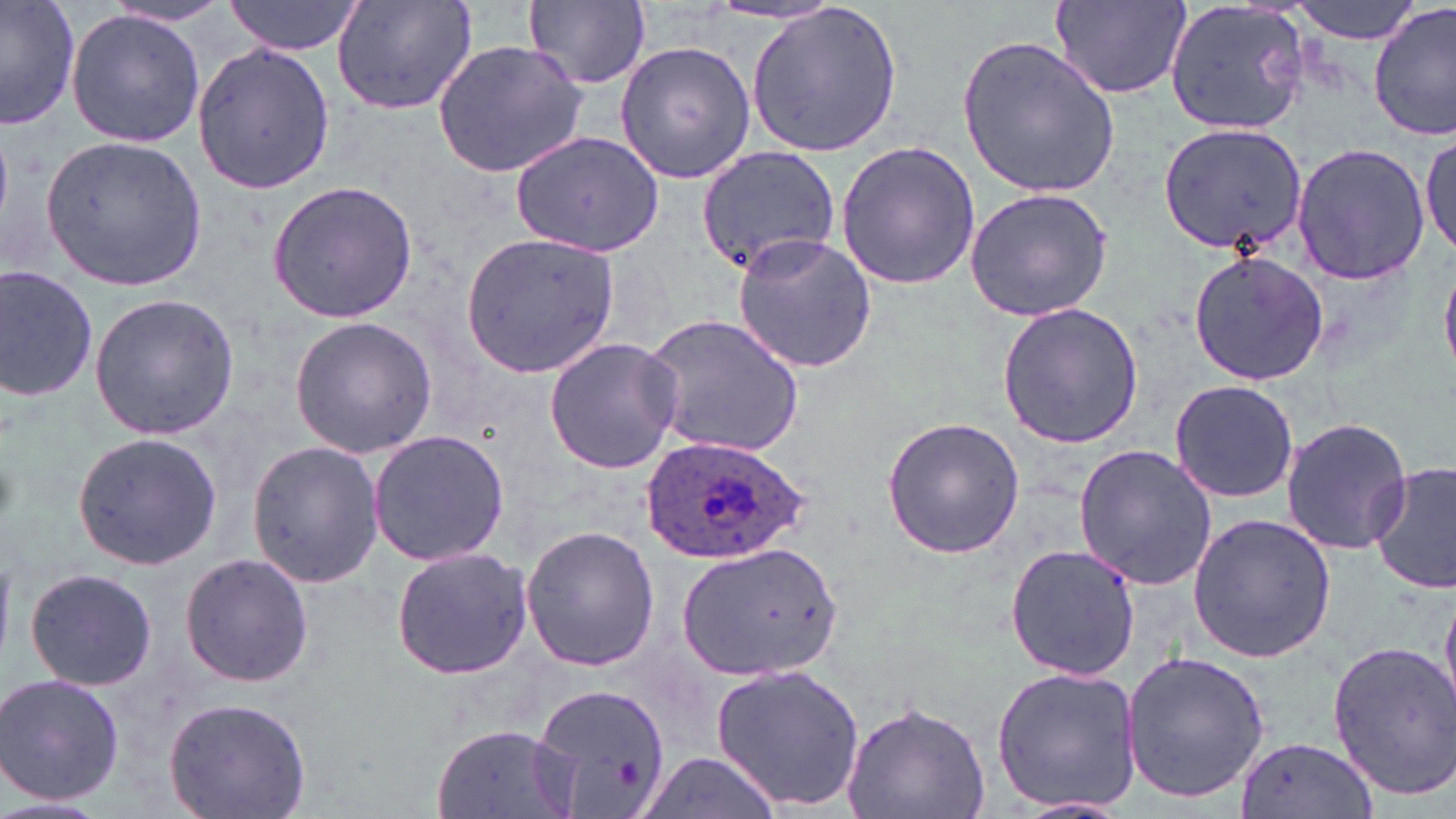
Approximate bounding boxes as [x1, y1, x2, y2] in pixels. Uninfected red blood cell locations: [0, 0, 78, 133], [223, 0, 369, 56], [332, 0, 480, 118], [1288, 0, 1424, 44], [99, 1, 235, 30], [522, 1, 654, 93], [1164, 1, 1313, 137], [1051, 2, 1190, 99], [746, 4, 904, 157], [1371, 4, 1455, 141], [66, 10, 206, 147], [956, 35, 1119, 200], [614, 38, 757, 184], [431, 39, 590, 178], [191, 42, 335, 196], [1157, 121, 1307, 255], [511, 129, 665, 256], [1419, 130, 1454, 261], [38, 132, 209, 292], [834, 140, 982, 291], [1290, 142, 1431, 286], [692, 144, 841, 277], [266, 180, 417, 323], [963, 187, 1115, 323], [460, 231, 621, 377], [732, 234, 879, 373], [1189, 250, 1331, 387], [0, 266, 98, 401], [87, 293, 241, 441], [995, 301, 1143, 449], [644, 313, 807, 457], [289, 315, 438, 459], [543, 336, 682, 474], [1168, 380, 1298, 502], [882, 417, 1025, 559], [1282, 418, 1413, 555], [367, 428, 511, 567], [70, 429, 223, 571], [245, 441, 384, 588], [1072, 444, 1219, 589], [1369, 461, 1456, 596], [1187, 513, 1337, 663], [521, 525, 660, 670], [677, 540, 844, 681], [1004, 542, 1141, 681], [390, 545, 535, 681], [178, 551, 315, 689], [25, 567, 157, 691], [1439, 591, 1456, 708], [1327, 642, 1456, 797], [1120, 650, 1273, 804], [711, 660, 864, 812], [990, 665, 1142, 813], [1, 673, 125, 806], [533, 682, 669, 819], [164, 698, 311, 819], [839, 698, 991, 819], [430, 724, 580, 819], [1233, 734, 1378, 819], [638, 753, 782, 819], [1000, 796, 1139, 817]. Plasmodium ovale-infected red blood cell locations: [641, 435, 809, 566]. Slide-level diagnosis: Plasmodium ovale. May-Grünwald-Giemsa stain. 1000x magnification. Image is 1456×819 pixels. Single field of view. Light microscopy. Thin blood smear.